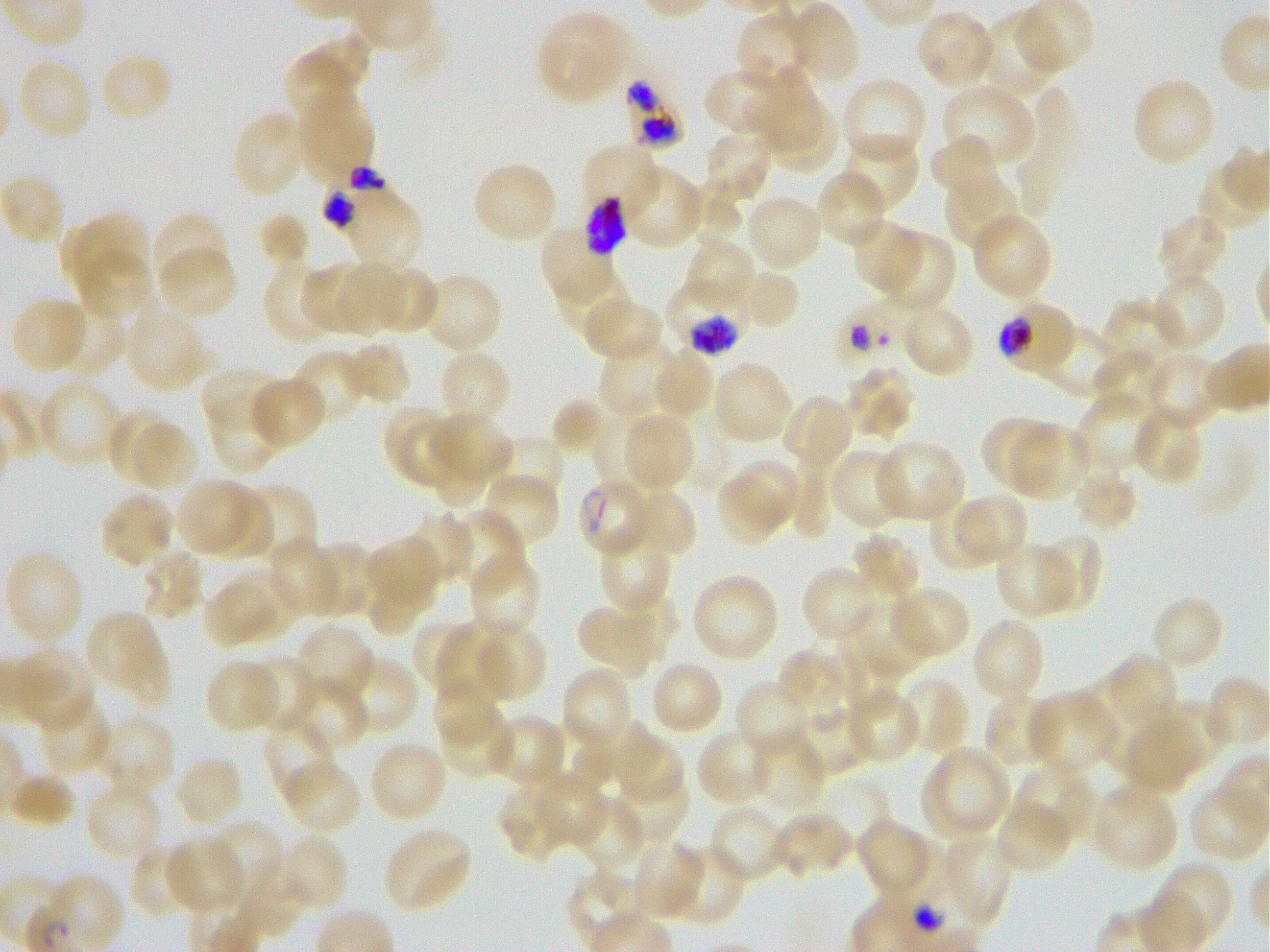
Not every red blood cell is marked. A life-cycle stage — or a range of stages, where the recorded stages span more than one — follows each staged infected red blood cell.
culture: in-vitro Plasmodium falciparum strain 3D7, static
field_of_view: single
preparation: thin blood film
stain: Giemsa
image_size: 1270×952 pixels
locations_of_uninfected_red_blood_cells: 'approximate bounding boxes as {x1, y1, x2, y2} in pixels: {787, 2, 861, 86}, {735, 9, 817, 93}, {915, 9, 997, 91}, {536, 10, 633, 106}, {978, 10, 1060, 98}, {284, 35, 370, 125}, {98, 51, 175, 123}, {16, 56, 94, 142}, {702, 68, 801, 139}, {748, 71, 824, 150}, {1131, 76, 1218, 168}, {840, 77, 927, 167}, {940, 83, 1035, 170}, {294, 86, 375, 186}, {1010, 89, 1084, 218}, {767, 105, 838, 171}, {231, 109, 309, 198}, {703, 128, 773, 206}, {840, 133, 919, 214}, {930, 134, 1006, 206}, {586, 146, 662, 225}, {471, 161, 559, 245}, {619, 164, 707, 251}, {815, 169, 888, 251}, {942, 172, 1021, 250}, {326, 179, 421, 272}, {678, 183, 743, 240}, {744, 192, 824, 272}, {151, 211, 229, 292}, {970, 211, 1053, 302}, {60, 212, 148, 296}, {1158, 212, 1231, 287}, {258, 213, 311, 270}, {851, 219, 925, 296}, {539, 224, 617, 306}, {876, 231, 955, 313}, {681, 236, 756, 312}, {156, 244, 238, 320}, {74, 248, 153, 323}, {262, 258, 338, 345}, {337, 263, 405, 340}, {371, 263, 439, 333}, {300, 265, 368, 333}, {555, 265, 643, 353}, {731, 270, 800, 330}, {1150, 271, 1227, 354}, {419, 272, 503, 355}, {9, 296, 90, 373}, {581, 297, 666, 364}, {1101, 299, 1189, 375}, {48, 300, 125, 377}, {899, 303, 976, 379}, {123, 304, 210, 393}, {1024, 317, 1121, 399}, {597, 340, 678, 418}, {338, 341, 412, 407}, {651, 347, 714, 420}, {1092, 348, 1168, 421}, {290, 349, 370, 426}, {438, 349, 513, 428}, {1144, 351, 1226, 430}, {711, 360, 794, 446}, {843, 365, 915, 442}, {200, 367, 289, 448}, {248, 375, 326, 451}, {37, 378, 124, 468}, {1075, 391, 1162, 473}, {209, 392, 297, 482}, {781, 393, 855, 474}, {552, 398, 613, 456}, {1130, 405, 1205, 486}, {384, 406, 449, 476}, {109, 408, 177, 481}, {594, 409, 666, 489}, {432, 411, 513, 477}, {981, 416, 1058, 492}, {623, 417, 694, 488}, {394, 420, 465, 486}, {134, 424, 198, 489}, {1010, 424, 1090, 502}, {486, 437, 564, 497}, {873, 440, 967, 524}, {432, 445, 491, 507}, {830, 448, 909, 530}, {788, 452, 834, 538}, {733, 460, 801, 527}, {1071, 464, 1138, 533}, {480, 469, 560, 549}, {717, 476, 780, 544}, {175, 479, 248, 553}, {232, 484, 318, 568}, {620, 486, 697, 561}, {199, 488, 274, 562}, {99, 489, 175, 568}, {955, 494, 1028, 561}, {929, 502, 999, 568}, {446, 509, 525, 593}, {403, 511, 473, 588}, {598, 527, 672, 613}, {853, 530, 923, 600}, {1030, 533, 1104, 614}, {367, 536, 442, 601}, {266, 539, 342, 618}, {994, 540, 1078, 619}, {307, 541, 377, 618}, {139, 547, 203, 621}, {1, 550, 83, 647}, {467, 551, 542, 637}, {800, 565, 880, 644}, {221, 568, 295, 643}, {690, 572, 781, 664}, {366, 575, 436, 636}, {203, 581, 275, 649}, {888, 584, 972, 660}, {623, 594, 680, 661}, {1149, 594, 1226, 672}, {848, 595, 926, 675}, {578, 608, 648, 679}, {83, 610, 171, 709}, {972, 618, 1047, 704}, {415, 620, 478, 695}, {471, 621, 547, 704}, {435, 622, 514, 706}, {293, 623, 376, 706}, {830, 643, 901, 723}, {9, 646, 95, 733}, {777, 648, 855, 721}, {1111, 653, 1180, 724}, {342, 655, 419, 737}, {246, 657, 319, 732}, {204, 659, 282, 734}, {648, 659, 724, 737}, {560, 667, 630, 744}, {1078, 671, 1158, 773}, {289, 676, 369, 753}, {434, 677, 502, 749}, {898, 677, 970, 756}, {736, 678, 815, 756}, {985, 688, 1062, 766}, {1027, 690, 1119, 776}, {850, 692, 922, 761}, {36, 697, 114, 776}, {783, 697, 874, 778}, {1160, 698, 1226, 770}, {438, 704, 515, 780}, {89, 714, 174, 796}, {488, 715, 563, 787}, {1125, 716, 1201, 794}, {263, 718, 337, 804}, {576, 721, 648, 784}, {695, 727, 774, 807}, {612, 729, 684, 808}, {747, 732, 826, 816}, {366, 740, 449, 824}, {919, 745, 1012, 842}, {171, 755, 244, 829}, {279, 760, 362, 835}, {1013, 762, 1097, 845}, {537, 770, 605, 847}, {611, 770, 687, 848}, {5, 772, 78, 829}, {84, 780, 164, 862}, {499, 783, 577, 859}, {1088, 783, 1179, 871}, {570, 795, 646, 876}, {994, 799, 1075, 876}, {708, 803, 792, 883}, {768, 812, 854, 879}, {855, 816, 933, 902}, {206, 820, 286, 907}, {383, 826, 472, 913}, {931, 832, 1010, 933}, {273, 833, 348, 916}, {164, 836, 246, 916}, {237, 837, 327, 937}, {629, 840, 705, 920}, {664, 842, 746, 926}, {129, 844, 199, 918}, {1154, 860, 1234, 945}'
objective: 100x, oil immersion, numerical aperture 1.25
locations_of_infected_red_blood_cells: 'approximate bounding boxes as {x1, y1, x2, y2} in pixels: {619, 68, 683, 156}; {663, 276, 748, 356} early trophozoite to early schizont; {997, 299, 1078, 378} trophozoite; {579, 480, 657, 559}'
locations_of_red_blood_cells_of_indeterminate_infection_status: 'approximate bounding boxes as {x1, y1, x2, y2} in pixels: {826, 282, 905, 369}'
donor_blood_group: O+